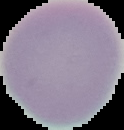 Result: no malaria parasites detected. The area outside the segmented cell region is set to black. Image is 124×130 pixels. From a thin blood smear.